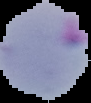 The area outside the segmented cell region is set to black. Malaria status: parasitized. From a thin blood smear. Image is 91×103 pixels.